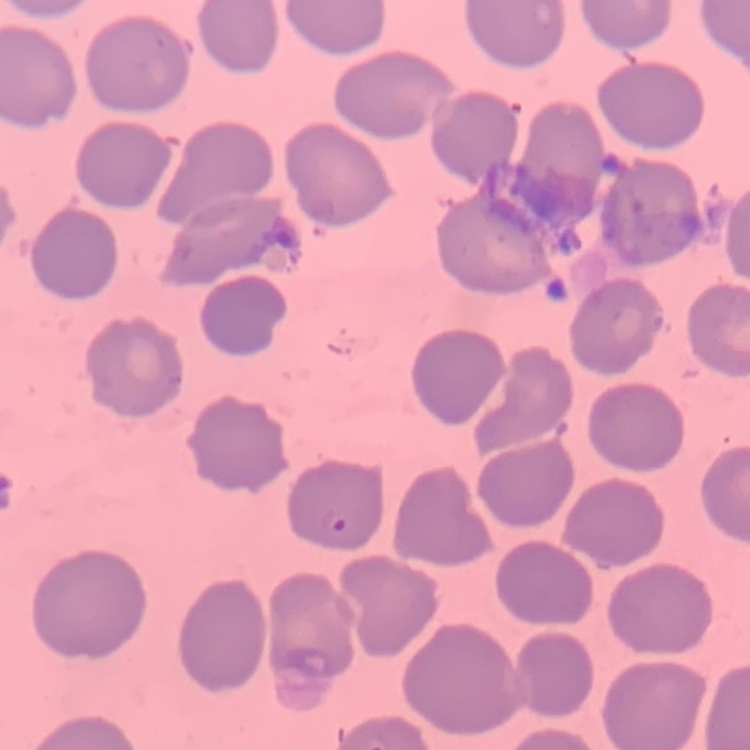
The erythrocytes exhibit no rouleaux formation. Thin blood smear. One tile cut from a larger photomicrograph. Stained with either Field's or Giemsa.